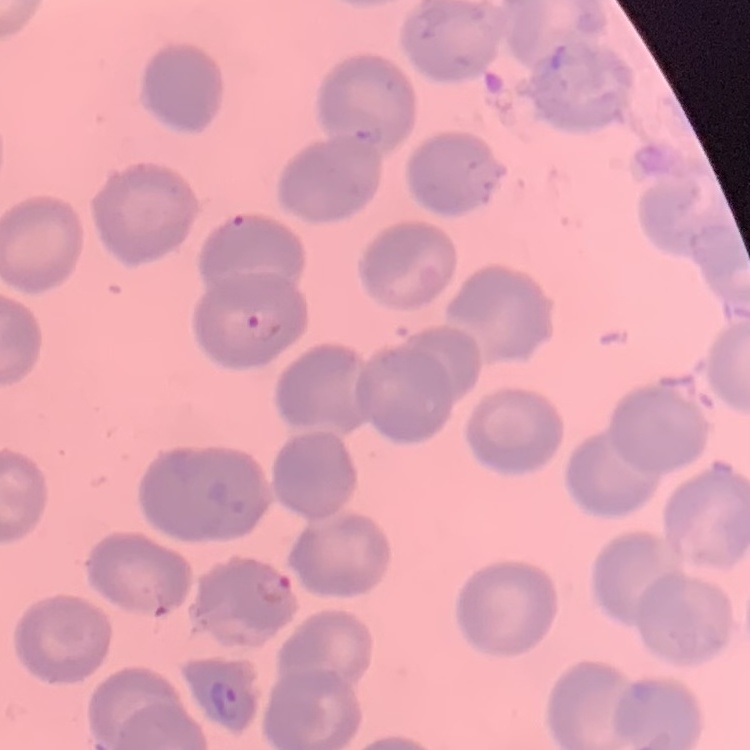

{
  "red_blood_cell_morphology": "no rouleaux formation",
  "stain": "Field's or Giemsa",
  "preparation": "thin blood film",
  "image_type": "square crop of a larger photomicrograph"
}